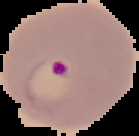

Summary:
  - Result: malaria parasites identified
  - Image size: 139×136 pixels
  - Image type: segmented cell region on a black background
  - Preparation: thin blood film